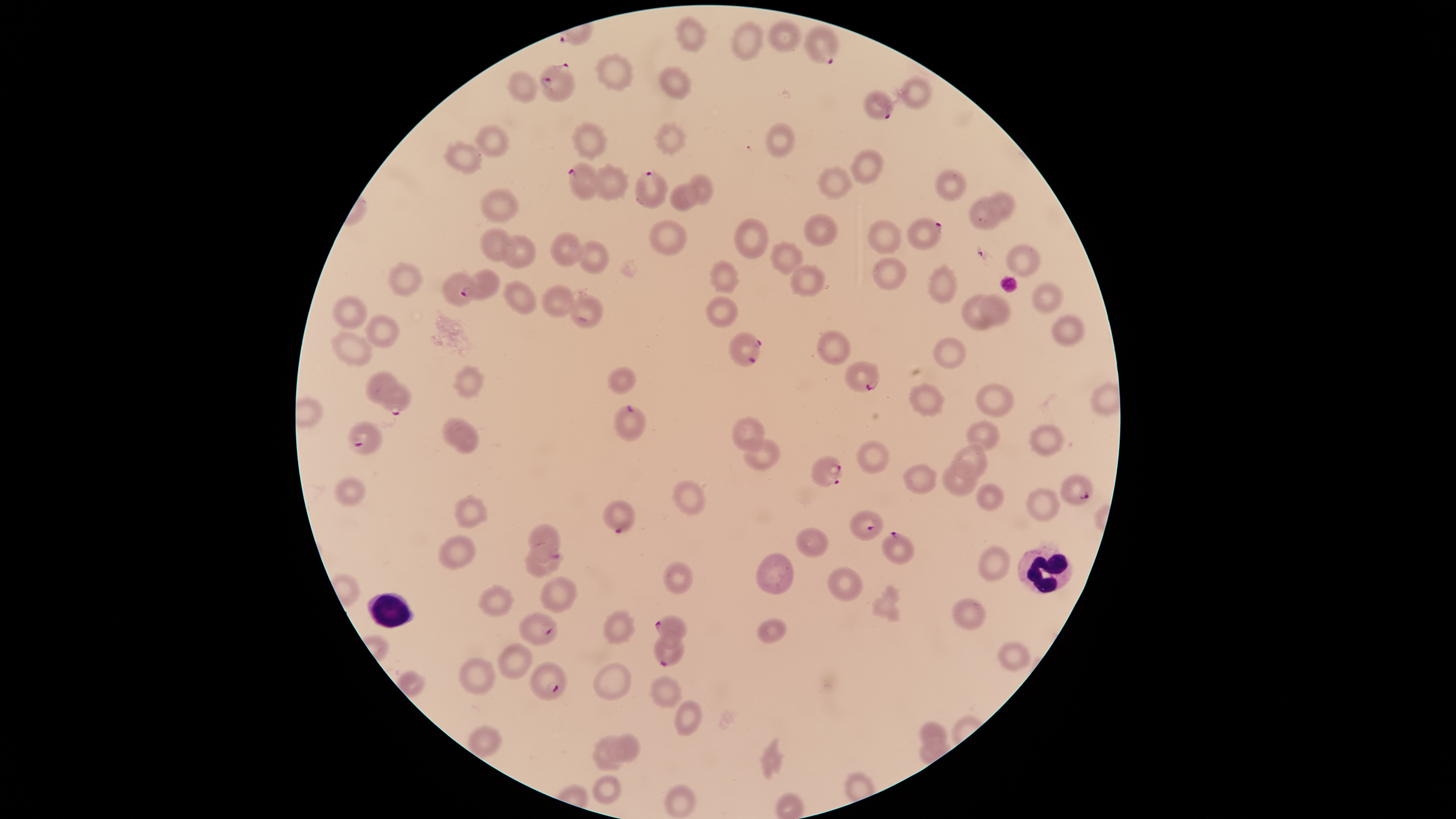

Approximate bounding boxes as (left, top, right, bottom) in pixels. Parasitized red blood cells: (804, 26, 838, 64), (539, 63, 575, 102), (864, 89, 894, 121), (567, 162, 600, 201), (635, 170, 669, 210), (906, 218, 943, 250), (460, 269, 500, 300), (728, 331, 763, 367), (845, 360, 880, 393), (377, 381, 411, 416), (613, 404, 646, 442), (347, 422, 383, 455), (811, 456, 843, 488), (1059, 475, 1095, 506), (603, 499, 635, 533), (849, 510, 884, 540), (528, 523, 560, 563), (881, 531, 914, 565), (518, 612, 559, 647), (655, 615, 688, 648), (655, 631, 684, 666), (529, 661, 567, 700). Uninfected red blood cells: (674, 16, 707, 52), (768, 18, 801, 52), (730, 20, 764, 60), (596, 54, 635, 89), (658, 67, 690, 98), (506, 71, 538, 101), (900, 76, 933, 108), (572, 122, 607, 157), (765, 123, 795, 157), (654, 124, 685, 152), (476, 125, 509, 157), (444, 141, 482, 172), (849, 149, 884, 183), (589, 167, 628, 199), (816, 167, 852, 199), (934, 169, 967, 201), (687, 172, 713, 203), (670, 183, 698, 211), (480, 188, 519, 223), (988, 191, 1016, 219), (967, 196, 1002, 229), (804, 213, 838, 246), (649, 219, 687, 256), (734, 219, 768, 259), (867, 219, 901, 254), (480, 228, 515, 263), (550, 232, 584, 267), (500, 235, 536, 269), (579, 241, 608, 273), (771, 241, 804, 275), (1006, 243, 1040, 276), (871, 257, 907, 289), (711, 260, 739, 292), (386, 263, 423, 297), (789, 264, 824, 296), (928, 266, 957, 303), (442, 272, 477, 307), (502, 280, 537, 314), (1031, 282, 1063, 312), (542, 284, 575, 318), (978, 293, 1013, 326), (961, 294, 997, 331), (569, 295, 604, 329), (331, 296, 368, 330), (706, 296, 738, 327), (365, 314, 400, 349), (1052, 315, 1085, 347), (816, 330, 851, 365), (329, 332, 372, 365), (932, 337, 966, 370), (455, 366, 483, 398), (607, 366, 635, 394), (364, 371, 399, 404), (974, 383, 1014, 418), (908, 384, 944, 416), (730, 416, 765, 451), (440, 418, 470, 446), (966, 420, 1000, 451), (449, 424, 479, 454), (1029, 424, 1065, 457), (742, 438, 782, 471), (856, 440, 890, 473), (953, 446, 988, 478), (942, 461, 979, 496), (902, 464, 937, 494), (333, 476, 367, 507), (674, 480, 705, 516), (975, 483, 1004, 511), (1026, 488, 1060, 521), (454, 496, 486, 528), (795, 527, 829, 557), (439, 534, 476, 571), (977, 545, 1010, 581), (523, 549, 564, 579), (757, 553, 795, 595), (664, 562, 693, 595), (829, 566, 863, 602), (542, 576, 577, 613), (479, 585, 514, 617), (952, 598, 986, 631), (603, 610, 634, 643), (757, 617, 786, 643), (998, 640, 1031, 672), (498, 643, 532, 679), (460, 658, 496, 695), (593, 662, 632, 701), (650, 675, 683, 708), (675, 699, 702, 736), (920, 721, 948, 756), (468, 725, 502, 758), (606, 733, 640, 763), (593, 736, 626, 772), (593, 775, 622, 805), (664, 784, 697, 818). White blood cells: (1017, 545, 1072, 594), (368, 593, 414, 628). Image is 1456×819 pixels. Giemsa stain. Thin blood film. Presence: malaria parasites identified. The visible region is circular. One field of view of the specimen. Species: Plasmodium falciparum. Smartphone photograph through the microscope eyepiece.